Classify this cell by malaria status.
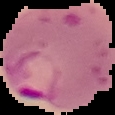

It is parasitized.

Summary:
  - Preparation: thin blood smear
  - Image type: segmented cell region on a black background
  - Image size: 115×115 pixels